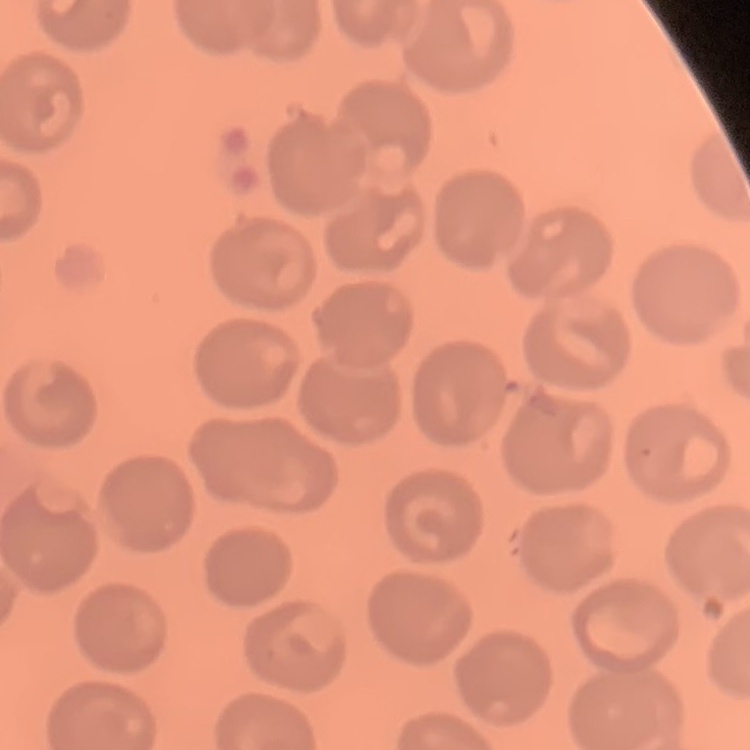
The erythrocytes exhibit no rouleaux formation. Thin blood smear. Square crop of a larger photomicrograph. Stained with either Field's or Giemsa.